Classify this cell by malaria status.
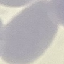

Uninfected.

Giemsa-stained preparation. Automatically extracted cell patch, resized to 64 × 64 pixels. Photographed with a smartphone camera at the microscope eyepiece. Thin smear of blood.